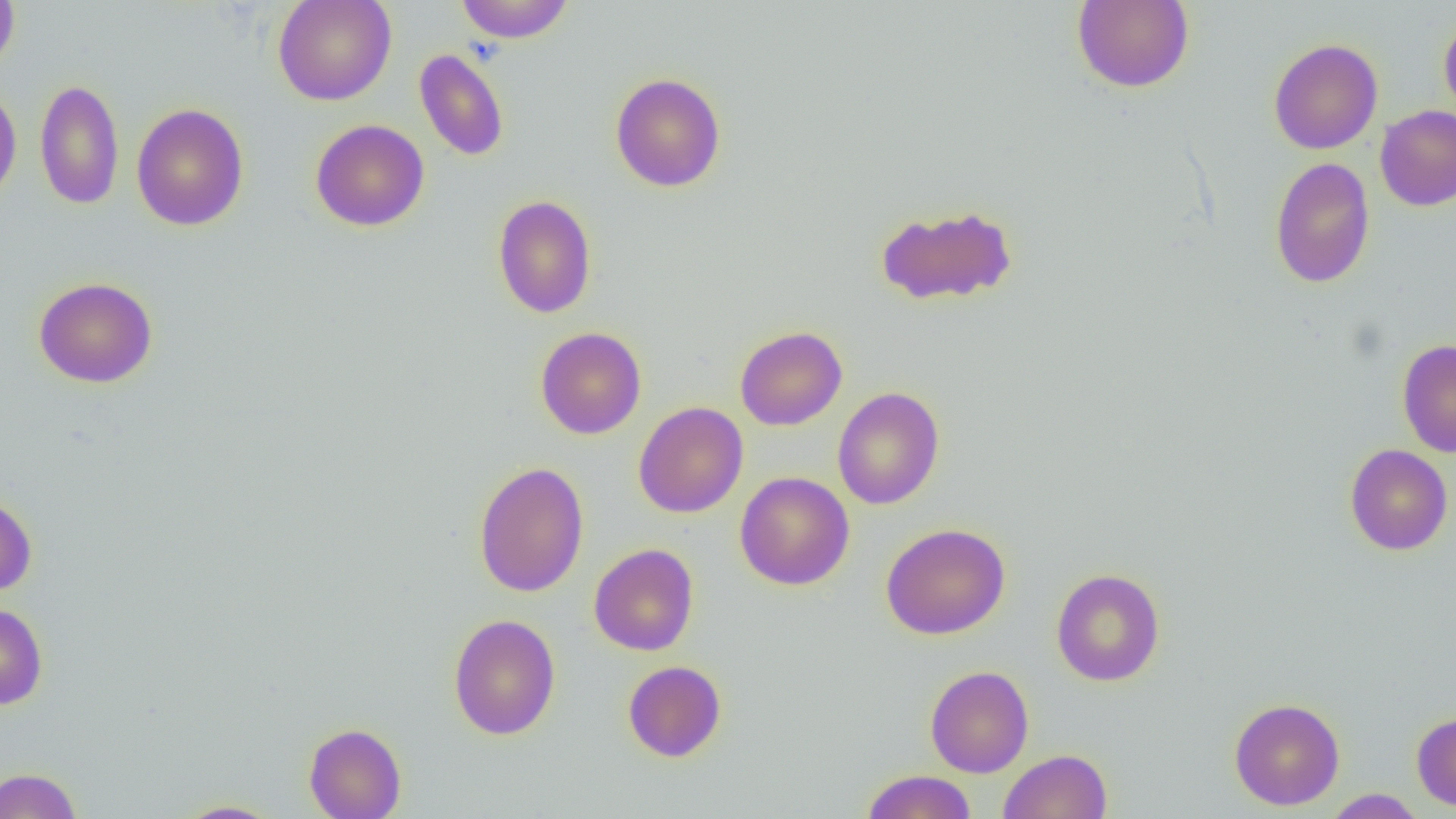
Approximate bounding boxes as (x1,y1)-(x2,y2) corner pairs in pixels. Uninfected red blood cell locations: (0,0)-(20,76), (272,0)-(397,106), (456,0)-(575,43), (1072,0)-(1194,93), (1439,15)-(1456,123), (1268,38)-(1383,154), (414,48)-(509,162), (610,72)-(727,192), (35,78)-(124,210), (0,82)-(22,207), (131,103)-(249,231), (1375,105)-(1456,211), (310,119)-(429,232), (1269,157)-(1375,288), (493,194)-(597,319), (874,203)-(1018,307), (33,276)-(158,389), (734,326)-(847,430), (535,327)-(646,439), (1397,338)-(1456,457), (832,387)-(945,510), (633,401)-(748,518), (1345,443)-(1453,556), (473,461)-(589,597), (735,471)-(855,590), (0,495)-(37,596), (881,522)-(1011,640), (588,542)-(699,655), (1051,568)-(1165,686), (0,602)-(48,710), (448,613)-(561,740), (622,660)-(726,763), (925,666)-(1034,778), (1229,698)-(1345,810), (1411,711)-(1456,812), (303,722)-(406,818), (998,749)-(1113,819), (0,767)-(83,819), (860,769)-(977,819), (1323,789)-(1426,818), (173,799)-(284,818). Slide-level diagnosis: negative for blood parasites. Thin blood film. Image is 1456×819 pixels. Optical microscopy. Captured at 1000x magnification. Single field of view.